Assess this cell for malaria.
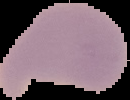

Uninfected.

Image is 130×100 pixels. From a thin blood smear. Segmented cell region on a black background.